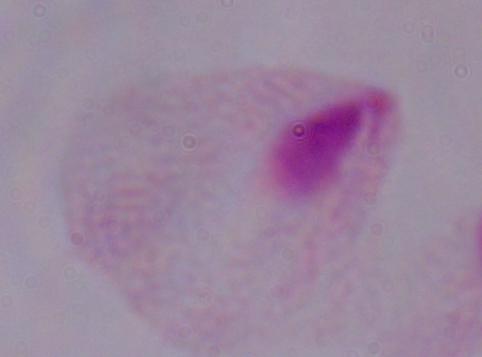

Summary:
  - Identification: trichomonad
  - Magnification: 1000x
  - Modality: micrograph